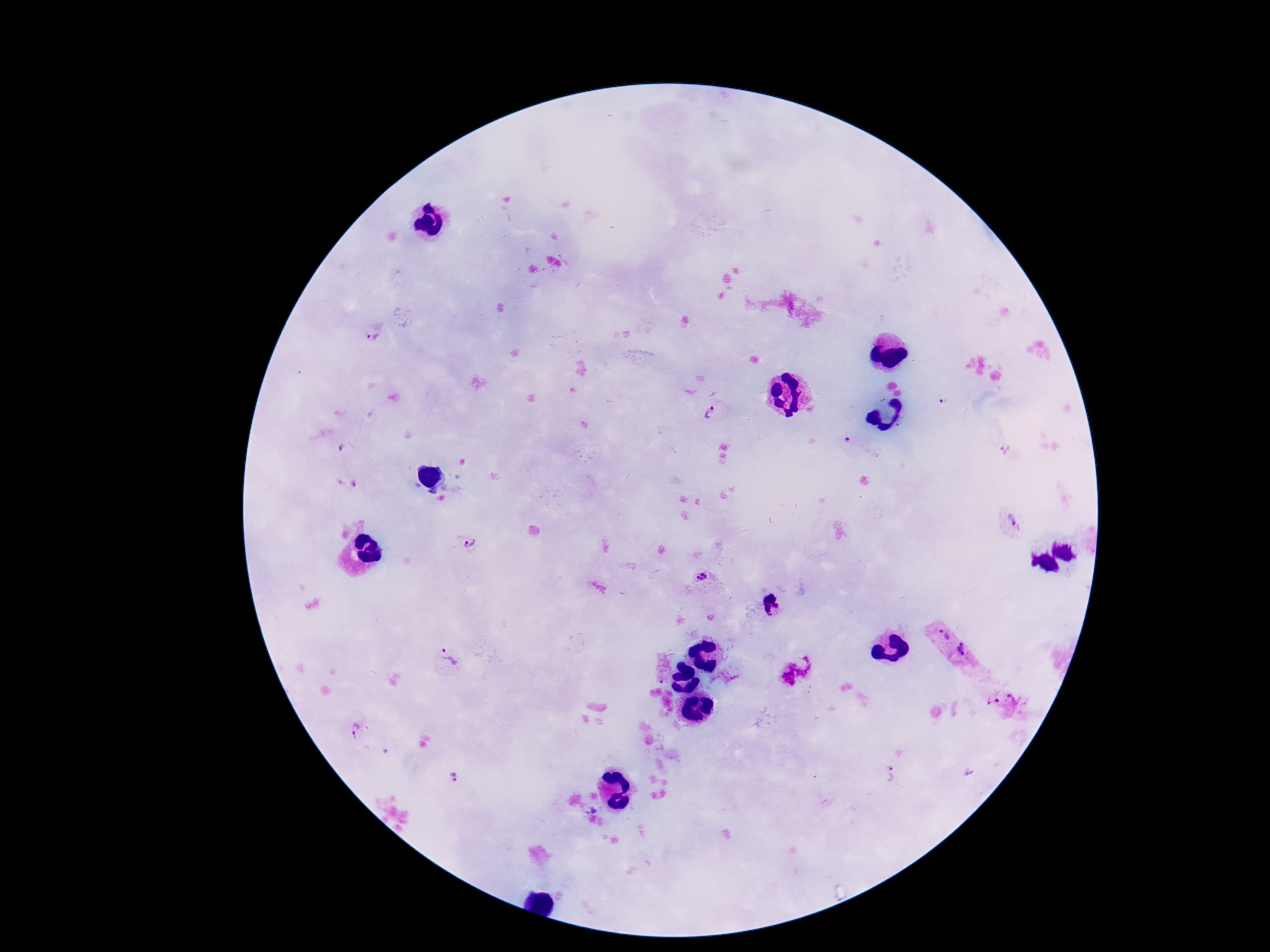

Approximate centers as {x, y} in pixels. Plasmodium parasite locations: {372, 335}, {711, 414}, {343, 449}, {1012, 520}, {472, 543}, {702, 576}, {944, 636}, {963, 649}, {450, 659}, {736, 678}, {995, 700}, {354, 731}, {890, 773}, {453, 776}. Thick blood smear. 100x magnification. Giemsa-stained preparation. Smartphone photograph taken through the microscope eyepiece. Single field of view. Patient malaria status: infected. Image is 1270×952 pixels.